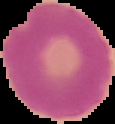
Image is 115×124 pixels. From a thin blood smear. Cell region segmented out of the field of view; the surrounding area is masked to black. Result: no malaria parasites seen.